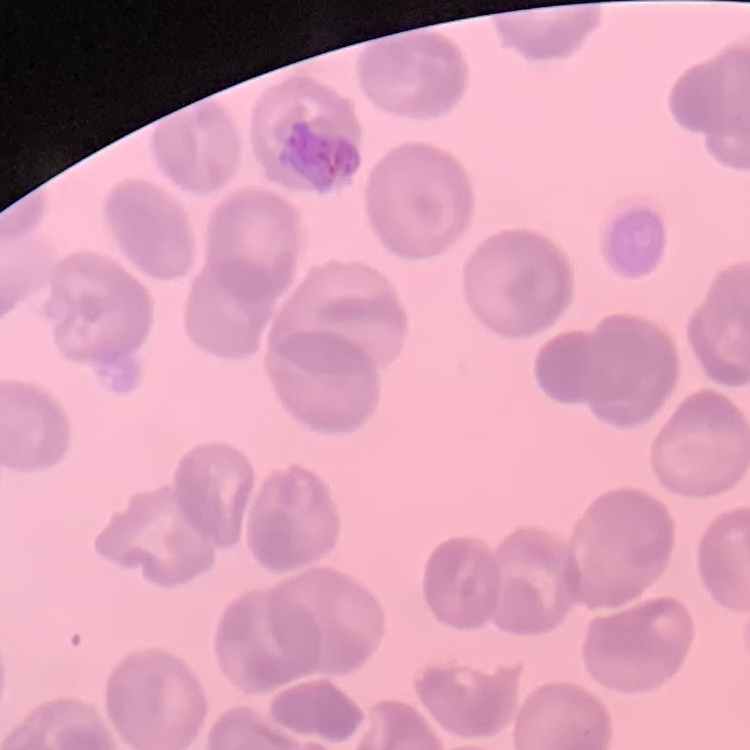
red blood cell morphology = no rouleaux formation
preparation = thin peripheral smear
stain = Field's or Giemsa
image type = square crop of a larger photomicrograph